Outline each Plasmodium ovale-infected red blood cell.
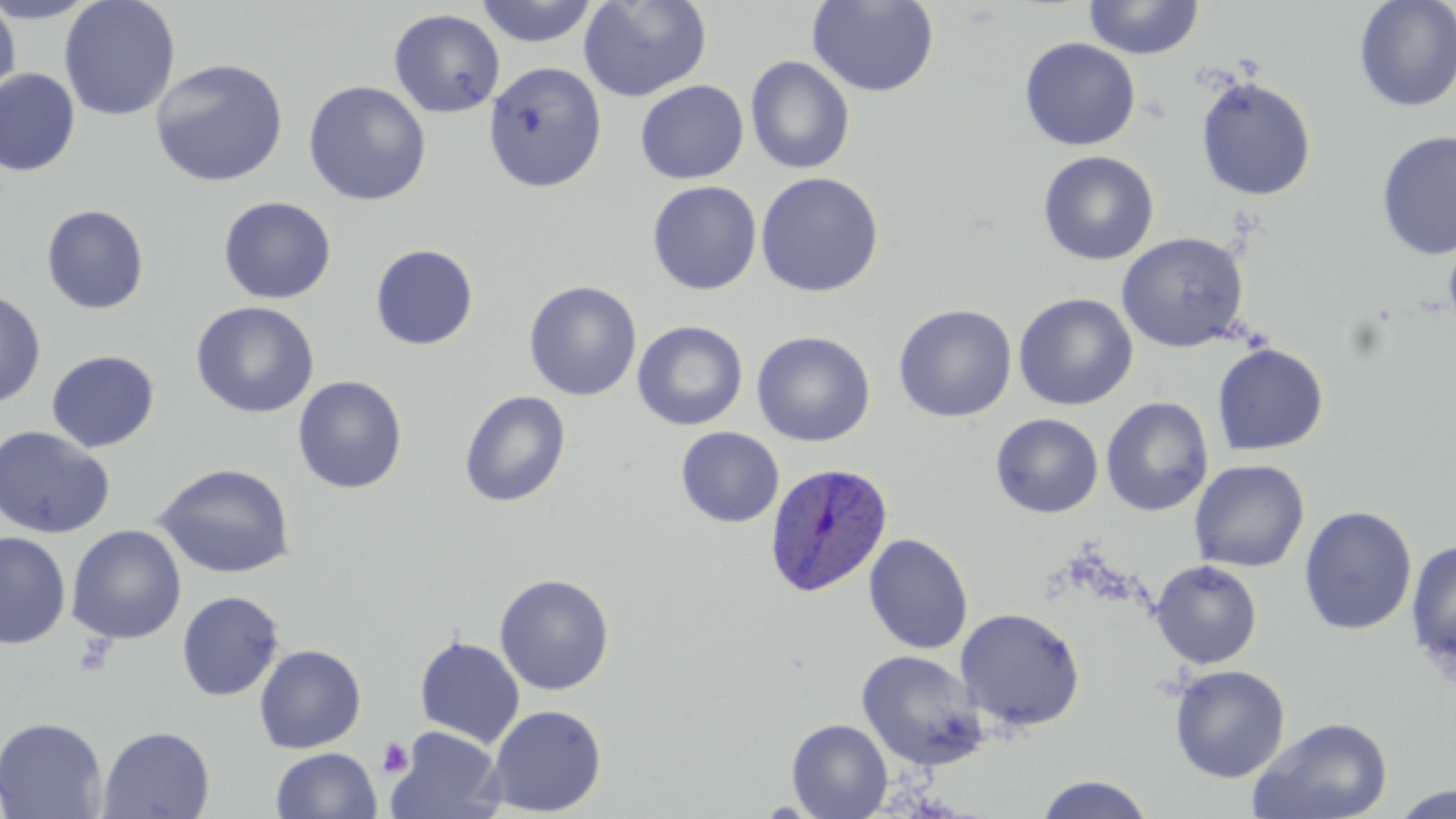

Approximate bounding boxes as [x1, y1, x2, y2] in pixels.
Plasmodium ovale-infected red blood cells: [764, 461, 893, 597].

Summary:
  - Platelet locations: [71, 635, 117, 679], [377, 736, 415, 778]
  - Uninfected red blood cell locations: [0, 0, 100, 23], [59, 0, 181, 121], [578, 0, 712, 102], [1083, 0, 1203, 60], [1354, 0, 1456, 112], [0, 1, 20, 104], [474, 1, 600, 47], [807, 1, 939, 97], [389, 8, 505, 118], [1019, 38, 1140, 150], [745, 55, 855, 175], [149, 58, 289, 187], [483, 62, 607, 193], [0, 68, 80, 177], [1195, 77, 1317, 201], [303, 80, 432, 206], [635, 80, 749, 185], [1376, 129, 1456, 261], [1037, 151, 1159, 265], [755, 172, 884, 297], [647, 181, 762, 295], [218, 197, 337, 304], [40, 204, 150, 315], [1116, 232, 1249, 353], [1443, 235, 1456, 335], [370, 244, 479, 350], [523, 280, 642, 401], [0, 288, 46, 409], [1013, 292, 1138, 411], [191, 301, 319, 418], [893, 304, 1017, 423], [632, 321, 748, 431], [751, 331, 875, 447], [1211, 343, 1329, 455], [46, 350, 160, 453], [293, 375, 408, 494], [459, 390, 572, 507], [1101, 397, 1214, 517], [991, 413, 1104, 518], [0, 425, 114, 539], [676, 426, 784, 528], [1189, 459, 1309, 573], [152, 462, 297, 579], [1298, 505, 1418, 635], [66, 524, 186, 645], [0, 532, 71, 649], [863, 533, 974, 654], [1406, 539, 1456, 670], [1150, 560, 1263, 669], [494, 573, 615, 695], [177, 591, 284, 701], [955, 607, 1086, 732], [414, 635, 525, 748], [253, 644, 367, 753], [856, 650, 988, 771], [1169, 664, 1290, 782], [484, 704, 607, 817], [0, 716, 108, 819], [1249, 716, 1395, 819], [787, 718, 892, 819], [97, 725, 215, 819], [386, 726, 502, 819], [271, 747, 381, 819], [1035, 774, 1155, 818], [1391, 785, 1455, 819]
  - Slide-level diagnosis: Plasmodium ovale
  - Modality: optical microscopy
  - Field of view: one of a larger specimen
  - Preparation: thin blood smear
  - Magnification: 1000x
  - Image size: 1456×819 pixels
  - Stain: May-Grünwald-Giemsa